State which parasite is depicted.
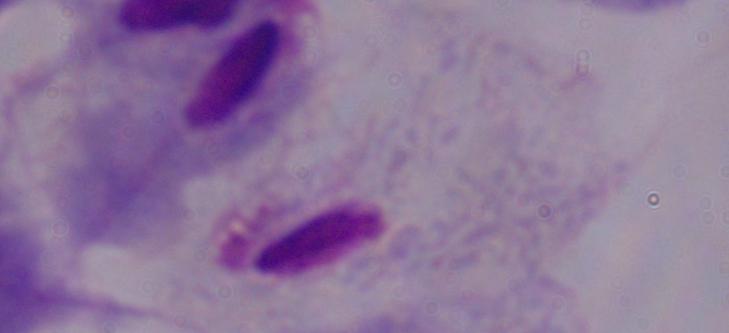

This is a trichomonad.

Summary:
  - Magnification: 1000x
  - Modality: micrograph